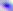

modality = micrograph
identification = Toxoplasma gondii
magnification = 400x